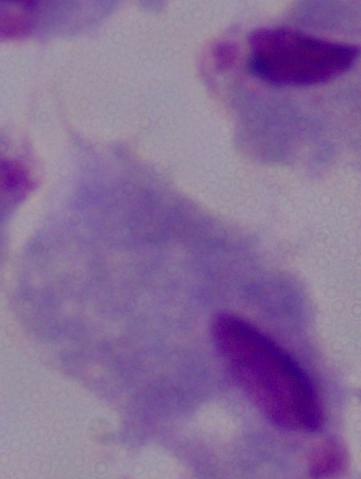

Summary:
  - Identification: trichomonad
  - Modality: photomicrograph
  - Magnification: 1000x